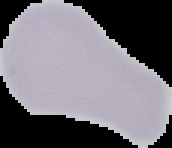 Image is 172×148 pixels. Result: no malaria parasites seen. From a thin blood film. Segmented cell region on a black background.